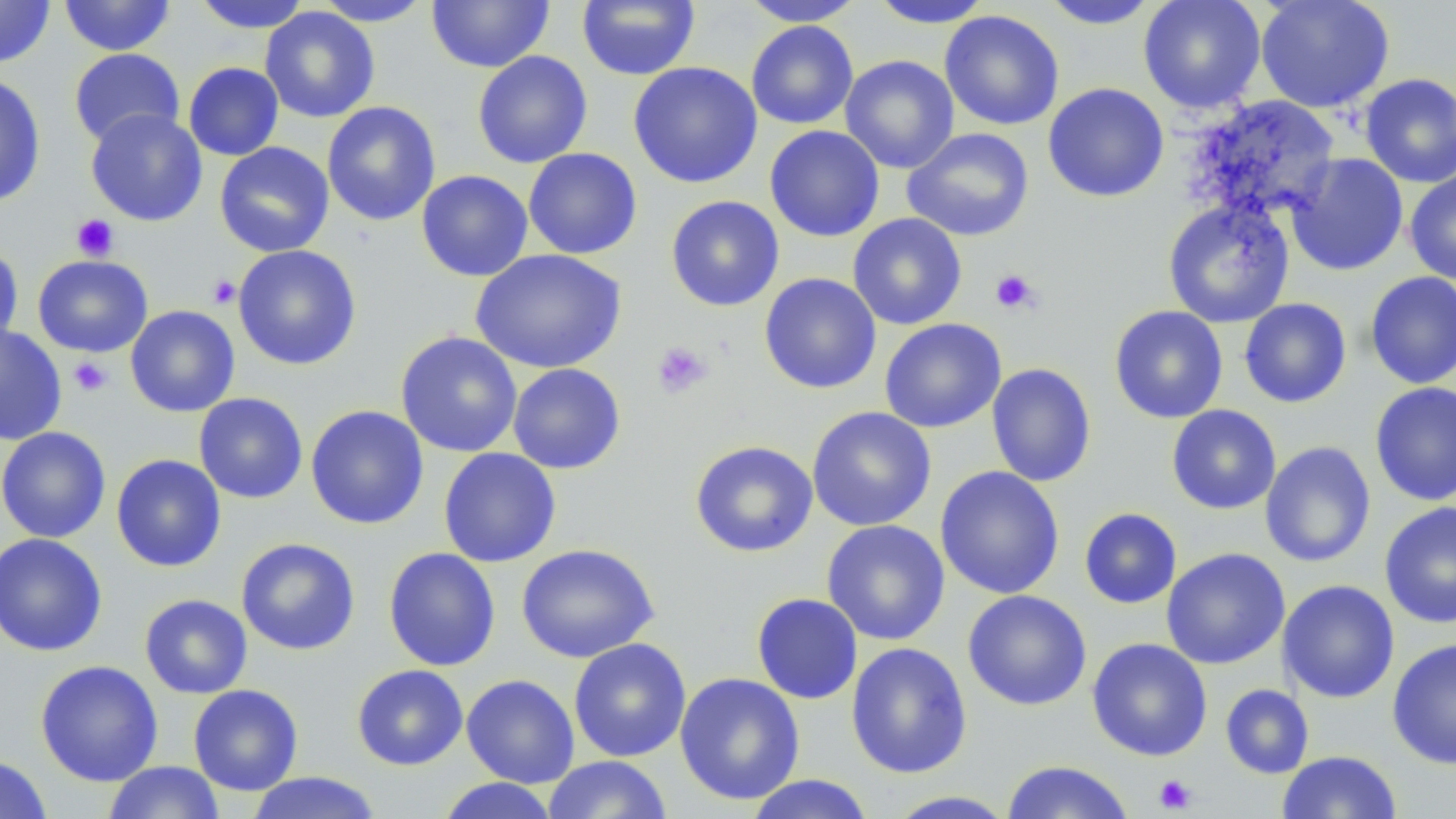

Summary:
  - Coordinate format: approximate bounding boxes as (x1,y1)-(x2,y2) corner pairs in pixels
  - Platelet locations: (72,214)-(119,261), (990,269)-(1040,314), (208,275)-(240,309), (651,341)-(713,399), (69,356)-(112,397), (1153,774)-(1197,814)
  - Uninfected red blood cell locations: (0,0)-(55,68), (59,0)-(176,56), (189,0)-(312,33), (312,0)-(435,26), (427,0)-(554,72), (577,0)-(700,81), (739,0)-(866,26), (1138,0)-(1266,114), (1255,0)-(1395,113), (868,1)-(996,29), (1037,1)-(1161,29), (260,6)-(380,123), (939,10)-(1065,131), (746,20)-(859,129), (68,48)-(185,149), (472,50)-(593,168), (840,54)-(959,174), (628,61)-(763,189), (183,62)-(284,161), (1360,72)-(1456,188), (0,73)-(47,207), (1042,83)-(1169,203), (1185,95)-(1341,223), (321,101)-(441,226), (85,108)-(208,226), (764,125)-(885,242), (901,127)-(1034,242), (214,142)-(335,257), (523,147)-(642,260), (1285,153)-(1408,276), (1404,168)-(1456,285), (416,170)-(533,281), (666,195)-(784,312), (1163,198)-(1295,328), (847,213)-(967,330), (0,244)-(24,353), (233,245)-(362,370), (470,249)-(628,374), (33,254)-(153,357), (1365,271)-(1456,389), (759,273)-(882,394), (1239,298)-(1352,408), (125,305)-(240,417), (1109,305)-(1228,424), (879,318)-(1006,433), (0,325)-(68,445), (395,331)-(523,457), (986,362)-(1097,487), (507,363)-(626,474), (1369,382)-(1456,506), (194,393)-(308,504), (305,405)-(429,529), (1166,405)-(1281,515), (807,406)-(936,531), (0,426)-(111,543), (689,440)-(819,558), (1260,441)-(1376,568), (0,442)-(227,554), (438,447)-(561,568), (111,453)-(226,572), (935,466)-(1065,599), (1379,501)-(1456,629), (1079,507)-(1182,609), (822,520)-(951,645), (0,533)-(107,657), (236,537)-(361,655), (517,542)-(659,662), (383,547)-(501,672), (1161,548)-(1290,669), (1278,579)-(1400,703), (962,589)-(1092,711), (751,593)-(863,705), (140,594)-(252,699), (569,638)-(691,762), (1087,638)-(1212,761), (1387,638)-(1456,770), (845,642)-(972,779), (35,660)-(163,786), (351,664)-(468,770), (675,672)-(805,805), (462,673)-(579,788), (188,684)-(303,795), (1220,684)-(1314,779), (1277,751)-(1402,818), (542,755)-(672,818), (0,756)-(52,819), (1000,760)-(1135,819), (102,761)-(226,819), (245,772)-(383,818), (743,774)-(876,819), (435,777)-(561,818), (881,790)-(1019,818)
  - Slide-level diagnosis: no evidence of blood parasites
  - Magnification: 1000x
  - Stain: May-Grünwald-Giemsa
  - Preparation: thin blood film
  - Field of view: one of a larger specimen
  - Image size: 1456×819 pixels
  - Modality: light microscopy